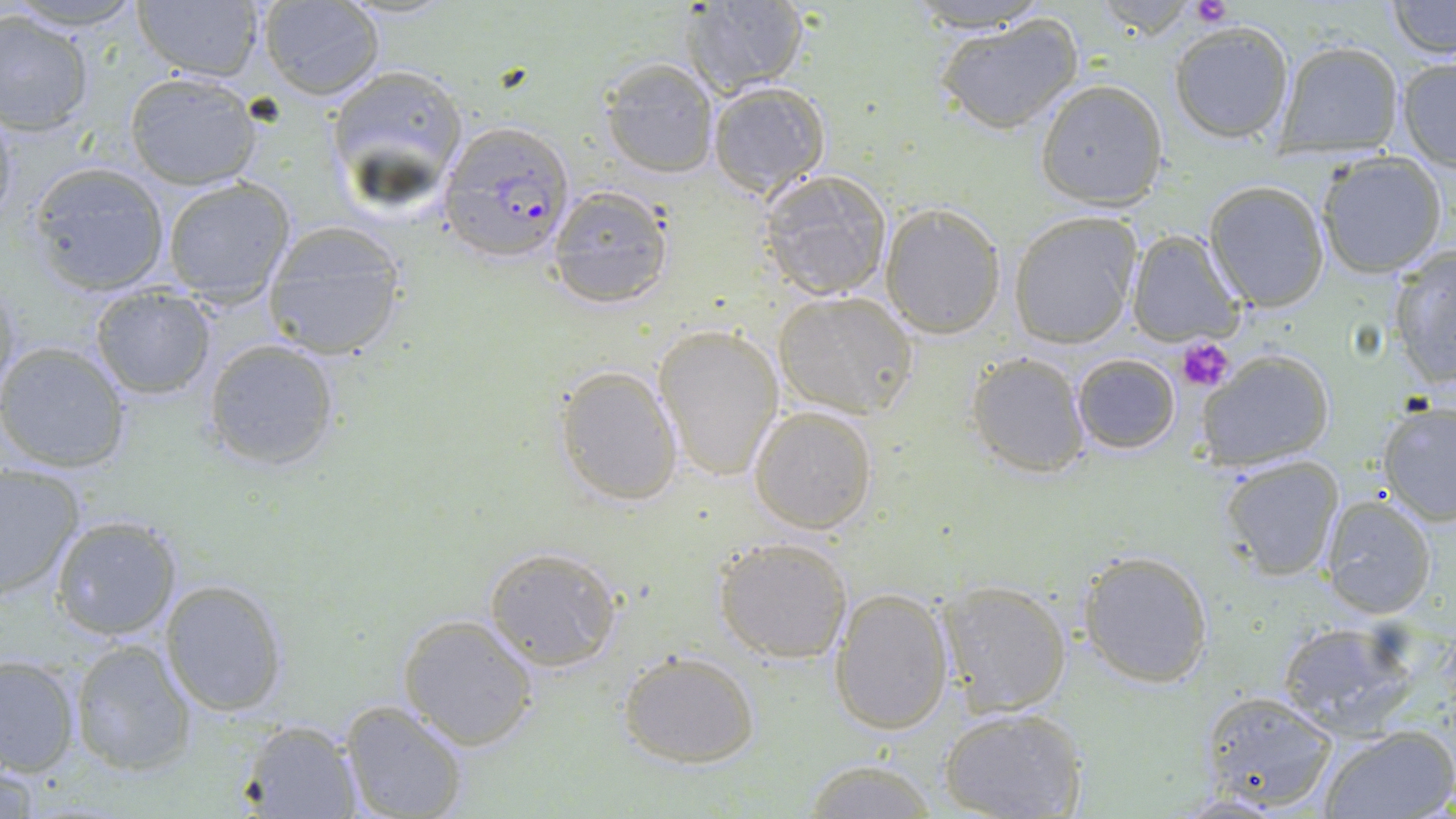
{
  "slide_level_diagnosis": "Plasmodium falciparum",
  "stain": "May-Grünwald-Giemsa",
  "uninfected_red_blood_cell_locations": "approximate bounding boxes as [x1, y1, x2, y2] in pixels: [0, 0, 153, 31], [904, 0, 1051, 31], [258, 1, 385, 100], [682, 1, 810, 96], [1088, 1, 1200, 42], [1386, 1, 1453, 59], [131, 2, 268, 83], [0, 10, 97, 135], [934, 12, 1085, 135], [1168, 19, 1296, 142], [1273, 40, 1405, 156], [1394, 56, 1456, 168], [599, 58, 719, 178], [321, 61, 470, 222], [123, 71, 264, 191], [707, 80, 832, 198], [1034, 80, 1169, 209], [1314, 152, 1448, 279], [25, 161, 172, 297], [759, 169, 893, 301], [161, 176, 298, 304], [1203, 180, 1329, 311], [547, 186, 672, 309], [880, 202, 1005, 338], [1009, 212, 1140, 348], [260, 221, 411, 360], [1130, 228, 1247, 347], [1387, 246, 1455, 390], [1, 276, 23, 398], [87, 283, 219, 401], [774, 289, 920, 418], [653, 323, 785, 483], [202, 337, 342, 472], [0, 342, 131, 472], [1197, 349, 1336, 470], [966, 351, 1089, 478], [1071, 352, 1180, 455], [553, 364, 683, 508], [1377, 400, 1456, 527], [748, 405, 879, 534], [1218, 454, 1345, 582], [1, 463, 84, 601], [1319, 494, 1437, 620], [49, 514, 184, 642], [714, 534, 855, 664], [483, 544, 623, 670], [1079, 549, 1216, 688], [160, 578, 290, 717], [935, 579, 1071, 718], [829, 587, 954, 736], [399, 615, 539, 751], [1276, 618, 1426, 737], [69, 638, 195, 775], [618, 649, 762, 768], [0, 655, 81, 778], [1193, 689, 1339, 811], [339, 699, 469, 819], [939, 706, 1087, 819], [239, 720, 364, 818], [1316, 725, 1455, 819], [803, 759, 940, 818]",
  "field_of_view": "single",
  "modality": "light microscopy",
  "preparation": "thin blood film",
  "image_size": "1456×819 pixels",
  "magnification": "1000x",
  "plasmodium_falciparum_infected_red_blood_cell_locations": "approximate bounding boxes as [x1, y1, x2, y2] in pixels: [439, 121, 574, 265]",
  "platelet_locations": "approximate bounding boxes as [x1, y1, x2, y2] in pixels: [1191, 0, 1232, 28], [1177, 336, 1234, 395]"
}